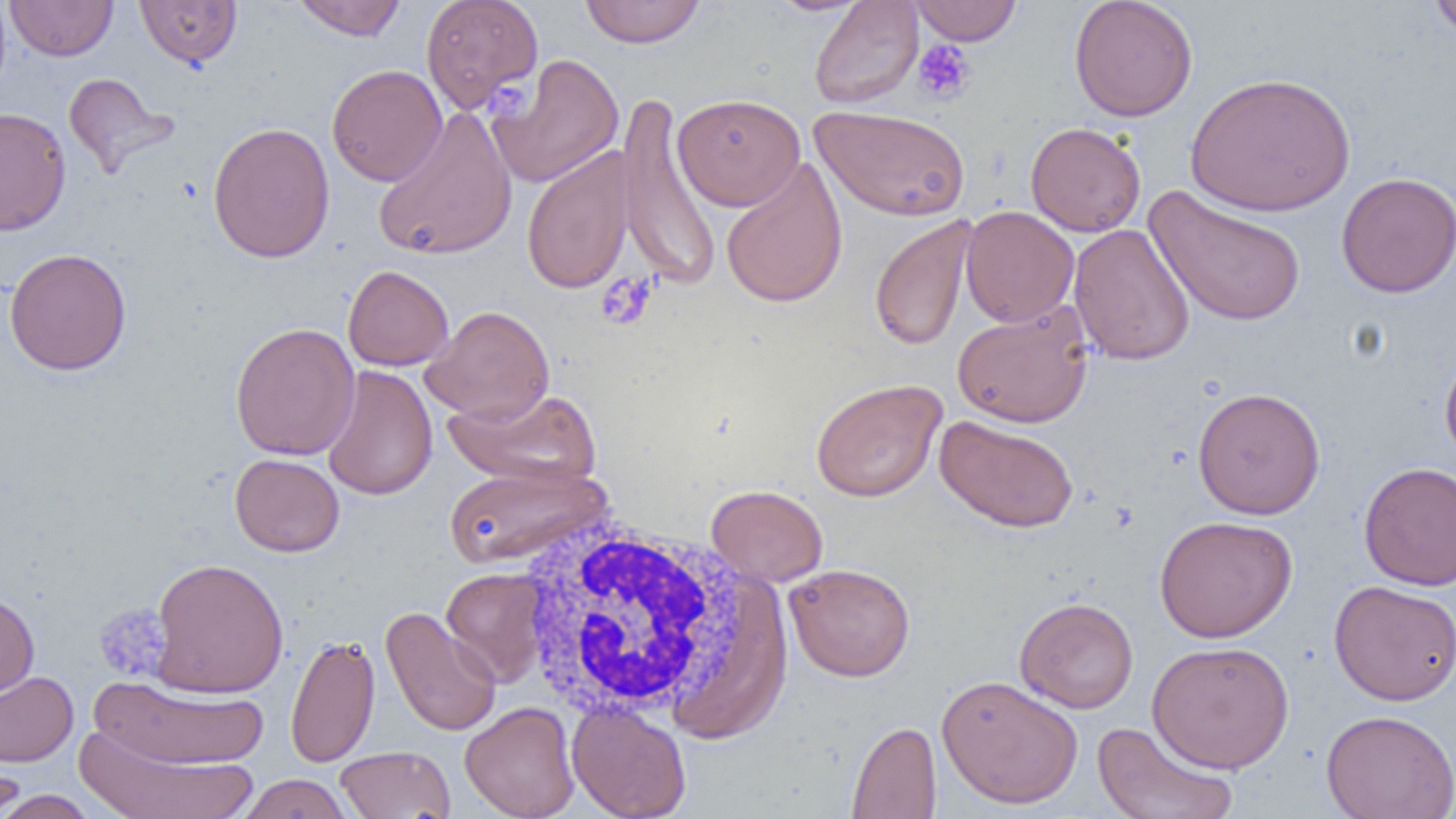

{
  "slide_level_diagnosis": "no evidence of blood parasites",
  "uninfected_red_blood_cell_locations": "approximate bounding boxes as (x1,y1)-(x2,y2) corner pairs in pixels: (134,0)-(242,69), (291,0)-(408,41), (420,0)-(544,115), (579,0)-(706,48), (767,0)-(873,16), (809,0)-(924,109), (909,0)-(1022,45), (1068,0)-(1198,122), (1427,0)-(1456,39), (5,1)-(117,61), (488,54)-(624,188), (327,64)-(447,186), (1185,71)-(1356,216), (63,72)-(176,176), (616,91)-(722,290), (673,93)-(805,211), (811,105)-(971,221), (0,106)-(71,235), (372,107)-(518,261), (207,121)-(336,264), (1025,122)-(1146,237), (521,147)-(636,295), (720,157)-(848,309), (1336,171)-(1456,298), (1144,186)-(1308,328), (960,205)-(1079,327), (868,213)-(979,353), (1068,223)-(1195,366), (3,248)-(132,376), (343,265)-(454,371), (951,301)-(1095,428), (421,305)-(555,424), (230,322)-(360,461), (1440,346)-(1456,468), (321,365)-(438,501), (810,378)-(947,502), (1192,386)-(1326,520), (444,387)-(601,488), (934,415)-(1079,533), (230,453)-(345,557), (1358,461)-(1456,591), (442,463)-(609,568), (706,484)-(828,587), (1154,515)-(1297,642), (150,557)-(289,698), (784,563)-(916,681), (440,567)-(551,687), (1329,580)-(1456,705), (0,592)-(39,701), (1014,597)-(1139,714), (380,606)-(502,737), (285,633)-(381,768), (1147,641)-(1295,773), (0,670)-(79,767), (936,674)-(1084,809), (89,676)-(271,770), (460,701)-(580,819), (567,703)-(691,819), (1321,709)-(1456,819), (846,720)-(942,818), (1090,720)-(1240,819), (74,726)-(259,819), (334,745)-(455,818), (0,750)-(26,819), (236,773)-(354,819), (0,790)-(101,819)",
  "field_of_view": "single",
  "white_blood_cell_locations": "approximate bounding boxes as (x1,y1)-(x2,y2) corner pairs in pixels: (513,513)-(756,722)",
  "platelet_locations": "approximate bounding boxes as (x1,y1)-(x2,y2) corner pairs in pixels: (913,39)-(976,105), (486,80)-(531,118), (595,271)-(658,331), (94,604)-(173,682)",
  "image_size": "1456×819 pixels",
  "magnification": "1000x",
  "preparation": "thin blood smear",
  "modality": "optical microscopy"
}